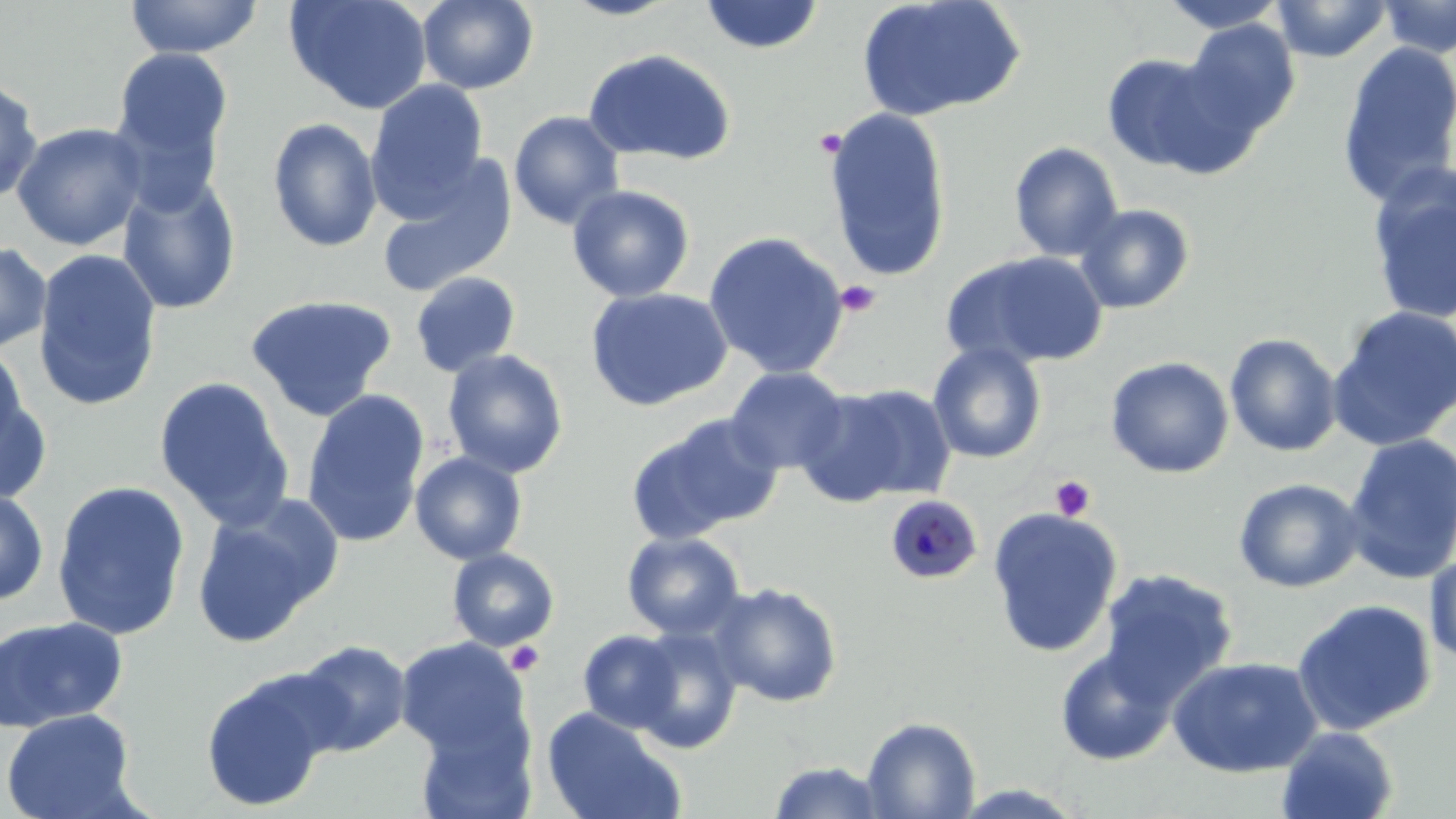
slide-level diagnosis = Plasmodium malariae
preparation = thin blood smear
magnification = 1000x
image size = 1456×819 pixels
stain = May-Grünwald-Giemsa
platelet locations = approximate bounding boxes as (x1,y1)-(x2,y2) corner pairs in pixels: (835,280)-(882,317), (1049,475)-(1096,521), (505,641)-(544,676)
Plasmodium malariae-infected red blood cell locations = approximate bounding boxes as (x1,y1)-(x2,y2) corner pairs in pixels: (885,494)-(983,585)
modality = light microscopy
field of view = single
uninfected red blood cell locations = approximate bounding boxes as (x1,y1)-(x2,y2) corner pairs in pixels: (124,0)-(262,60), (284,0)-(433,115), (417,0)-(539,95), (559,0)-(684,20), (698,0)-(825,55), (856,0)-(1026,122), (1157,0)-(1291,34), (1271,0)-(1393,62), (1378,0)-(1456,59), (1180,21)-(1300,140), (1336,42)-(1456,209), (111,48)-(233,172), (582,48)-(736,165), (1100,53)-(1236,175), (0,76)-(43,206), (365,79)-(490,217), (821,108)-(953,282), (508,111)-(625,230), (266,117)-(383,253), (12,122)-(148,252), (1008,142)-(1125,262), (376,154)-(518,299), (1365,165)-(1456,326), (116,174)-(241,315), (567,183)-(696,303), (1073,203)-(1196,314), (704,230)-(850,379), (0,241)-(52,353), (32,248)-(162,412), (941,250)-(1109,369), (410,271)-(521,378), (584,286)-(734,412), (244,294)-(398,421), (1329,305)-(1456,450), (1224,333)-(1343,458), (0,342)-(30,460), (928,342)-(1047,463), (441,348)-(570,478), (1106,356)-(1234,479), (1,361)-(48,505), (725,366)-(849,475), (153,376)-(295,531), (795,383)-(953,509), (300,389)-(430,549), (629,414)-(784,542), (1342,433)-(1456,584), (409,451)-(528,564), (1233,478)-(1366,593), (51,479)-(192,641), (0,487)-(49,607), (190,498)-(340,649), (987,507)-(1123,658), (621,531)-(746,640), (447,548)-(561,651), (1425,549)-(1456,670), (1098,568)-(1239,705), (707,582)-(844,708), (1291,598)-(1437,737), (0,615)-(128,733), (627,627)-(743,753), (578,629)-(686,735), (394,637)-(530,759), (292,639)-(412,756), (1053,645)-(1180,766), (1167,656)-(1322,778), (200,669)-(337,812), (0,707)-(140,819), (540,707)-(686,819), (862,716)-(981,818), (415,718)-(538,819), (1276,725)-(1399,819), (767,760)-(891,818)